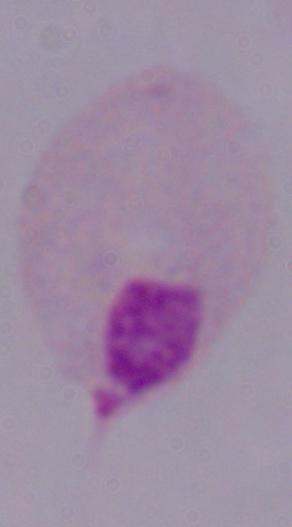
Summary:
  - Modality: micrograph
  - Magnification: 1000x
  - Identification: trichomonad